Give the extent of all Plasmodium ovale-infected red blood cells.
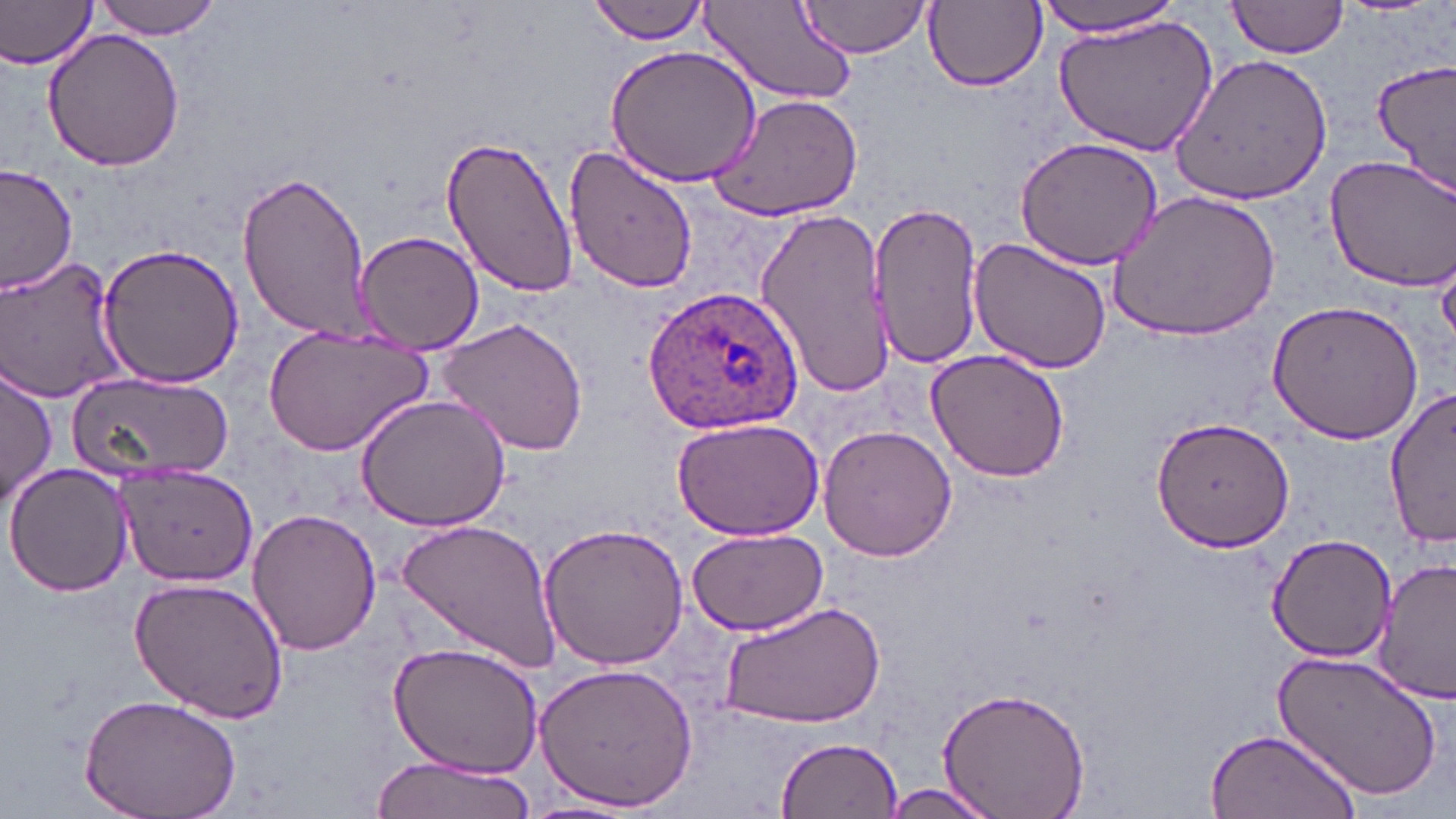
Approximate bounding boxes as [x1, y1, x2, y2] in pixels.
Plasmodium ovale-infected red blood cells: [642, 286, 805, 436].

Summary:
  - Uninfected red blood cell locations: [0, 0, 100, 71], [93, 0, 221, 40], [796, 0, 932, 58], [1034, 0, 1188, 37], [1224, 0, 1352, 59], [920, 1, 1048, 94], [590, 2, 711, 42], [700, 2, 859, 108], [1052, 14, 1220, 156], [41, 29, 187, 172], [603, 45, 761, 188], [1171, 54, 1334, 204], [1372, 60, 1456, 193], [706, 91, 864, 222], [440, 134, 580, 299], [1013, 138, 1164, 268], [561, 140, 700, 295], [1324, 155, 1456, 290], [0, 165, 76, 297], [235, 170, 373, 341], [1107, 190, 1282, 342], [870, 199, 984, 370], [753, 205, 893, 402], [355, 230, 486, 354], [968, 239, 1113, 375], [98, 241, 244, 389], [1, 254, 128, 403], [1266, 302, 1425, 445], [438, 317, 591, 457], [263, 325, 433, 454], [924, 349, 1070, 483], [2, 366, 57, 506], [68, 369, 232, 481], [1386, 387, 1455, 549], [355, 393, 512, 532], [671, 415, 826, 540], [1150, 415, 1296, 553], [817, 424, 957, 562], [6, 461, 133, 599], [116, 464, 258, 587], [246, 507, 383, 656], [398, 518, 560, 673], [538, 522, 690, 672], [685, 527, 828, 636], [1266, 532, 1400, 662], [1374, 558, 1456, 702], [128, 576, 290, 725], [718, 598, 887, 731], [387, 641, 546, 779], [1272, 646, 1444, 802], [533, 664, 698, 812], [934, 686, 1092, 819], [77, 692, 244, 819], [1203, 726, 1359, 819], [776, 738, 903, 818], [370, 754, 538, 819], [871, 782, 1005, 819], [519, 796, 649, 819]
  - Slide-level diagnosis: Plasmodium ovale
  - Field of view: one of a larger specimen
  - Image size: 1456×819 pixels
  - Stain: May-Grünwald-Giemsa
  - Preparation: thin blood film
  - Modality: optical microscopy
  - Magnification: 1000x